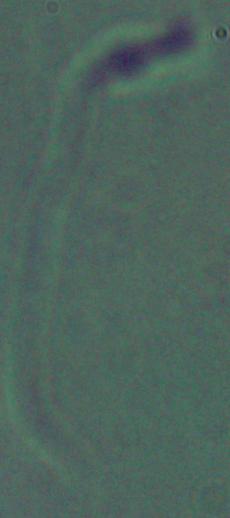
A Leishmania parasite is seen. Captured at 1000x magnification. Photomicrograph.